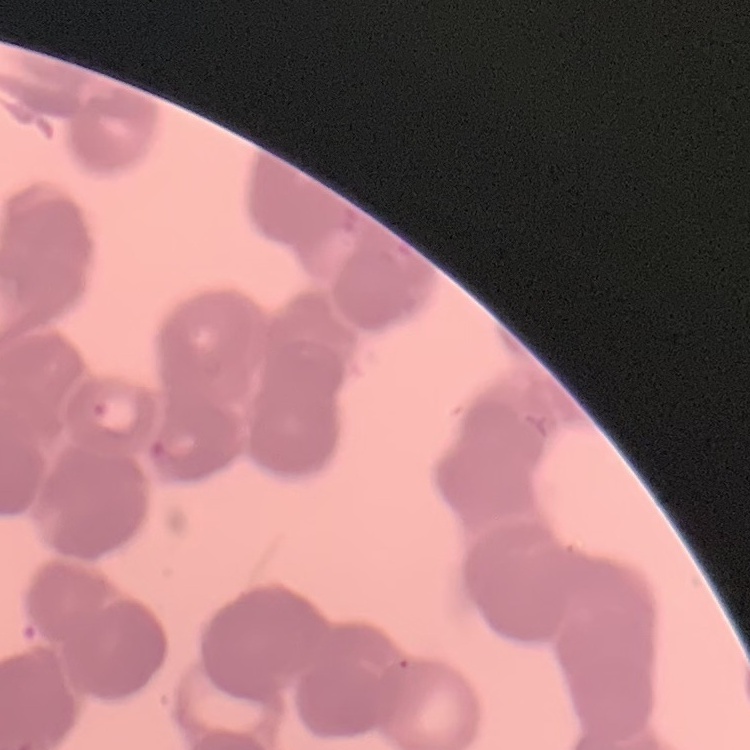 The red blood cells show rouleaux formation. Square crop of a larger photomicrograph. Field's or Giemsa stain. Thin peripheral smear.